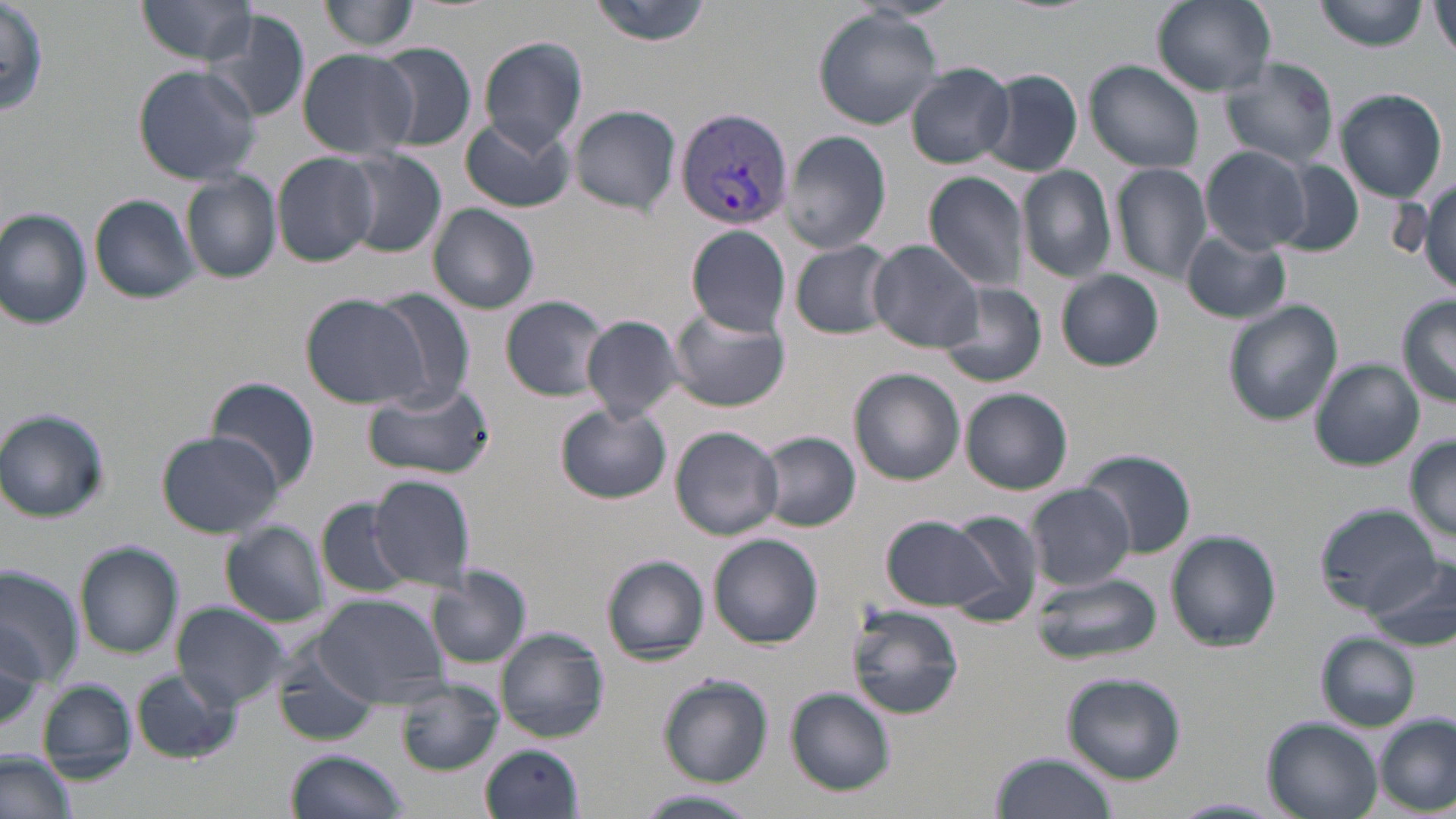
Approximate bounding boxes as (x1, y1, x2, y2) in pixels. Uninfected red blood cell locations: (0, 0, 48, 117), (134, 0, 262, 64), (319, 0, 417, 54), (588, 0, 714, 46), (1152, 0, 1277, 95), (1315, 0, 1426, 51), (1433, 1, 1456, 60), (813, 9, 945, 129), (205, 10, 311, 124), (479, 38, 587, 151), (371, 42, 477, 151), (297, 48, 417, 161), (1219, 56, 1339, 169), (1083, 61, 1204, 172), (131, 63, 261, 185), (907, 64, 1015, 168), (980, 68, 1083, 178), (1334, 87, 1448, 202), (569, 104, 680, 214), (461, 117, 577, 212), (781, 131, 892, 254), (1200, 146, 1315, 255), (341, 149, 448, 259), (272, 153, 380, 266), (1272, 158, 1365, 259), (1111, 163, 1211, 282), (1018, 165, 1117, 283), (182, 172, 282, 284), (924, 172, 1028, 292), (902, 187, 1021, 357), (90, 193, 201, 305), (427, 204, 539, 314), (1, 208, 94, 331), (687, 225, 792, 335), (1182, 229, 1291, 324), (789, 239, 895, 340), (867, 241, 986, 352), (1057, 270, 1164, 371), (937, 282, 1046, 388), (374, 291, 474, 406), (300, 293, 431, 409), (502, 294, 614, 401), (1397, 295, 1456, 405), (1222, 300, 1344, 426), (666, 306, 790, 412), (581, 315, 687, 423), (1310, 358, 1424, 470), (848, 368, 965, 485), (208, 376, 321, 494), (366, 382, 494, 481), (961, 388, 1073, 494), (557, 404, 671, 505), (0, 410, 110, 522), (670, 425, 785, 540), (157, 429, 285, 539), (758, 433, 861, 533), (1405, 436, 1456, 543), (1077, 449, 1197, 560), (370, 475, 478, 586), (1025, 484, 1135, 590), (316, 499, 414, 598), (1317, 507, 1443, 619), (937, 508, 1045, 621), (880, 514, 1002, 612), (220, 521, 327, 626), (1166, 531, 1281, 653), (708, 534, 824, 648), (75, 544, 185, 657), (602, 554, 710, 662), (1369, 554, 1456, 651), (0, 565, 82, 688), (429, 567, 531, 668), (1027, 570, 1161, 665), (314, 593, 447, 708), (171, 602, 294, 708), (848, 604, 966, 719), (0, 616, 51, 733), (496, 628, 610, 743), (1316, 634, 1421, 730), (274, 645, 384, 748), (132, 670, 240, 764), (1061, 671, 1186, 783), (658, 676, 772, 785), (395, 679, 503, 774), (37, 680, 135, 782), (784, 687, 896, 797), (1006, 701, 1181, 813), (1261, 716, 1381, 819), (1375, 716, 1454, 814), (480, 744, 585, 819), (285, 750, 408, 818), (0, 751, 78, 819), (989, 751, 1119, 819), (633, 789, 764, 819), (1169, 798, 1285, 817). Plasmodium vivax-infected red blood cell locations: (676, 108, 794, 229). Slide-level diagnosis: Plasmodium vivax. Image is 1456×819 pixels. Captured at 1000x magnification. One field of a larger specimen. Light microscopy. May-Grünwald-Giemsa-stained preparation. Thin blood film.